Describe the morphology of the erythrocytes.
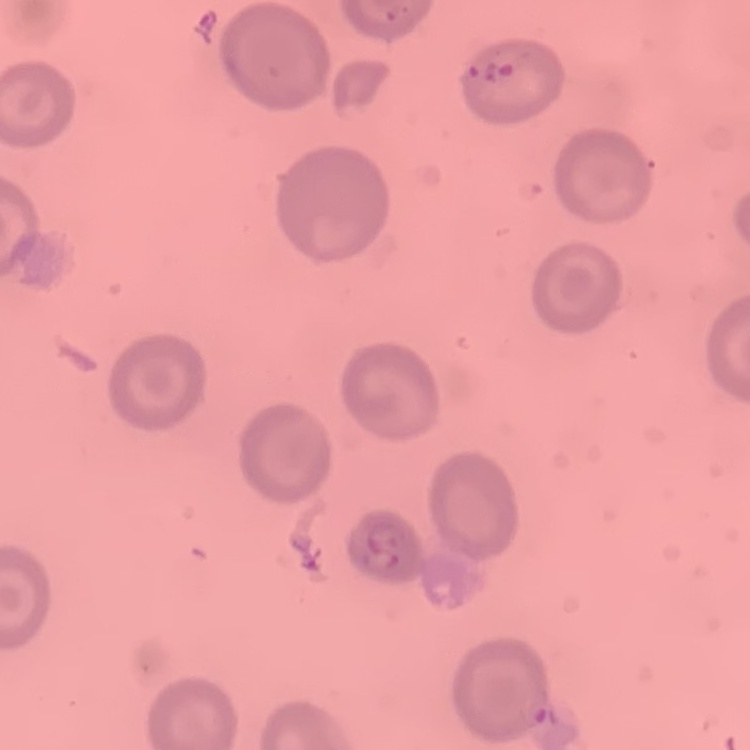
They show no rouleaux formation.

Summary:
  - Preparation: thin blood film
  - Image type: one tile cut from a larger photomicrograph
  - Stain: Field's or Giemsa